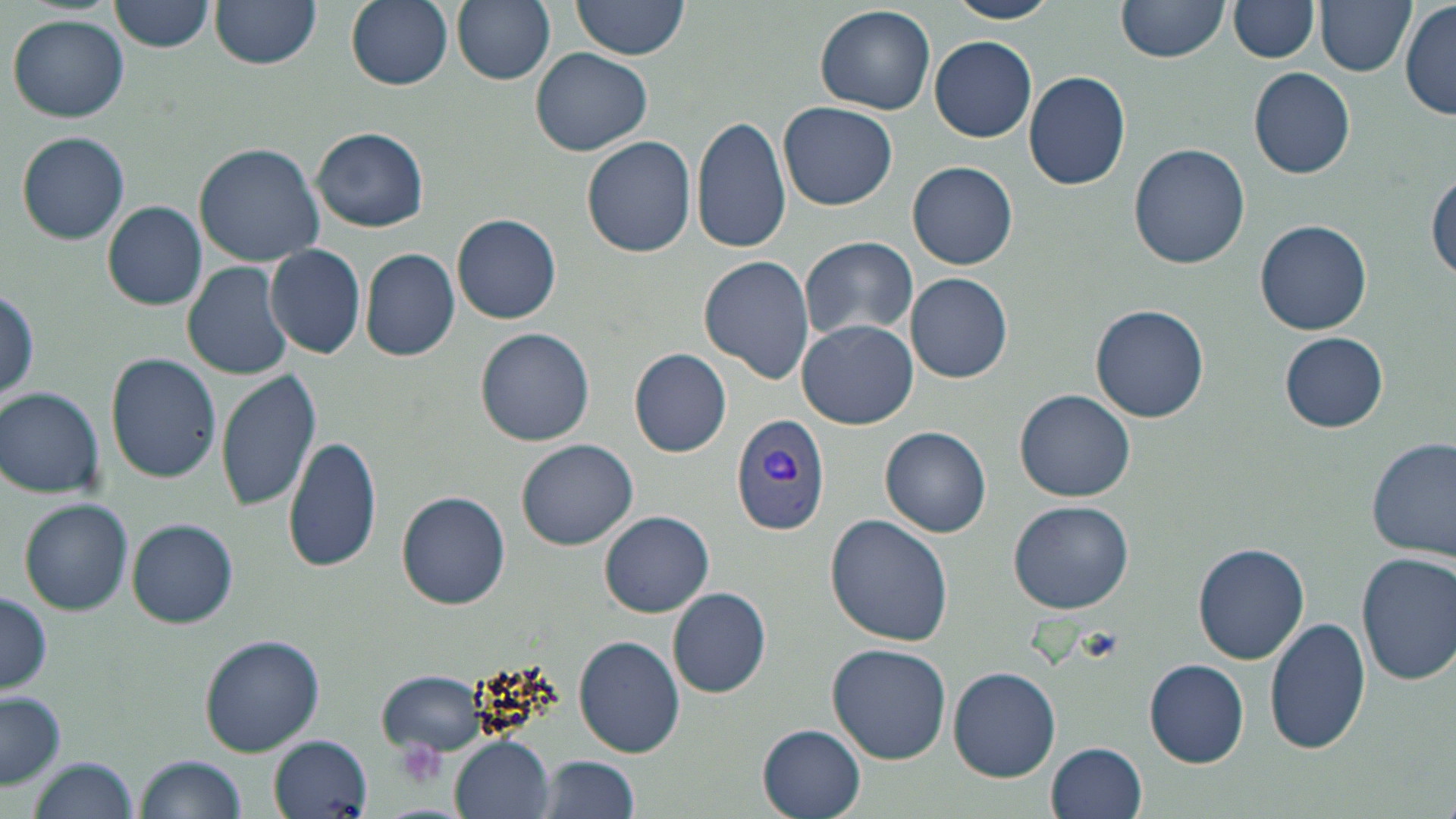
Summary:
  - Coordinate format: approximate bounding boxes as named x1/y1/x2/y2 corners in pixels
  - Plasmodium vivax-infected red blood cell locations: (x1=732, y1=412, x2=832, y2=534)
  - Platelet locations: (x1=398, y1=739, x2=446, y2=789)
  - Uninfected red blood cell locations: (x1=207, y1=0, x2=324, y2=69), (x1=342, y1=0, x2=455, y2=90), (x1=454, y1=0, x2=555, y2=85), (x1=569, y1=0, x2=690, y2=63), (x1=945, y1=0, x2=1059, y2=24), (x1=1317, y1=0, x2=1416, y2=76), (x1=109, y1=1, x2=214, y2=51), (x1=1230, y1=1, x2=1320, y2=62), (x1=1115, y1=2, x2=1229, y2=65), (x1=814, y1=3, x2=936, y2=115), (x1=1400, y1=4, x2=1455, y2=120), (x1=8, y1=16, x2=129, y2=122), (x1=929, y1=35, x2=1038, y2=143), (x1=530, y1=47, x2=655, y2=157), (x1=1249, y1=67, x2=1356, y2=179), (x1=1024, y1=70, x2=1132, y2=192), (x1=778, y1=102, x2=899, y2=210), (x1=693, y1=113, x2=790, y2=255), (x1=311, y1=127, x2=428, y2=232), (x1=16, y1=131, x2=130, y2=244), (x1=583, y1=136, x2=696, y2=257), (x1=194, y1=142, x2=326, y2=265), (x1=1129, y1=142, x2=1252, y2=269), (x1=907, y1=160, x2=1019, y2=270), (x1=1429, y1=172, x2=1455, y2=284), (x1=101, y1=200, x2=208, y2=310), (x1=453, y1=213, x2=562, y2=324), (x1=1254, y1=220, x2=1373, y2=336), (x1=800, y1=236, x2=917, y2=342), (x1=266, y1=244, x2=366, y2=359), (x1=360, y1=248, x2=460, y2=361), (x1=699, y1=254, x2=815, y2=385), (x1=182, y1=261, x2=294, y2=380), (x1=907, y1=272, x2=1015, y2=383), (x1=1, y1=287, x2=41, y2=405), (x1=1090, y1=304, x2=1212, y2=423), (x1=798, y1=319, x2=917, y2=429), (x1=476, y1=327, x2=596, y2=446), (x1=1281, y1=332, x2=1388, y2=433), (x1=629, y1=348, x2=733, y2=457), (x1=106, y1=351, x2=222, y2=483), (x1=217, y1=368, x2=320, y2=510), (x1=1, y1=388, x2=105, y2=498), (x1=1015, y1=390, x2=1135, y2=502), (x1=880, y1=426, x2=991, y2=538), (x1=282, y1=433, x2=382, y2=575), (x1=1367, y1=435, x2=1455, y2=561), (x1=517, y1=438, x2=638, y2=550), (x1=396, y1=491, x2=511, y2=610), (x1=19, y1=497, x2=133, y2=615), (x1=1008, y1=500, x2=1133, y2=613), (x1=600, y1=510, x2=714, y2=617), (x1=824, y1=514, x2=952, y2=648), (x1=127, y1=518, x2=238, y2=629), (x1=1193, y1=542, x2=1309, y2=665), (x1=1357, y1=552, x2=1456, y2=685), (x1=668, y1=586, x2=771, y2=698), (x1=0, y1=588, x2=52, y2=699), (x1=1264, y1=618, x2=1371, y2=759), (x1=198, y1=634, x2=325, y2=756), (x1=574, y1=634, x2=686, y2=757), (x1=827, y1=642, x2=952, y2=764), (x1=1145, y1=659, x2=1248, y2=767), (x1=949, y1=666, x2=1061, y2=781), (x1=377, y1=671, x2=489, y2=758), (x1=0, y1=693, x2=66, y2=790), (x1=758, y1=722, x2=868, y2=819), (x1=270, y1=733, x2=372, y2=816), (x1=451, y1=735, x2=555, y2=819), (x1=1046, y1=742, x2=1148, y2=819), (x1=135, y1=753, x2=247, y2=819), (x1=538, y1=755, x2=643, y2=819), (x1=28, y1=759, x2=139, y2=818)
  - Slide-level diagnosis: Plasmodium vivax
  - Image size: 1456×819 pixels
  - Stain: May-Grünwald-Giemsa
  - Field of view: one of a larger specimen
  - Modality: light microscopy
  - Preparation: thin blood smear
  - Magnification: 1000x